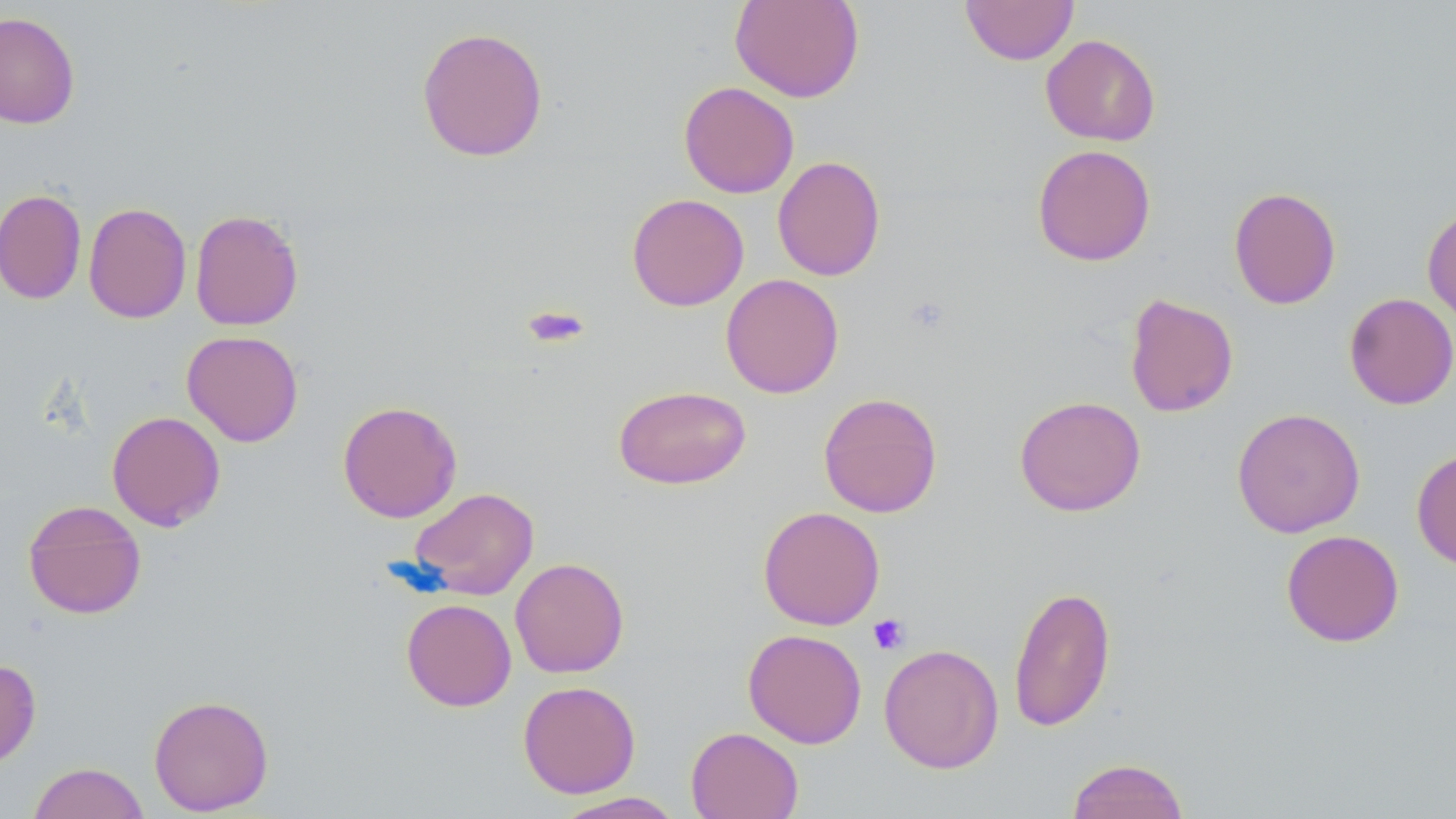
slide_level_diagnosis: no evidence of blood parasites
modality: optical microscopy
preparation: thin blood smear
magnification: 1000x
uninfected_red_blood_cell_locations: 'approximate bounding boxes as (x1,y1)-(x2,y2) corner pairs in pixels: (730,0)-(864,103), (960,0)-(1079,65), (0,11)-(80,129), (416,25)-(549,162), (1040,34)-(1161,146), (678,81)-(799,198), (1032,144)-(1156,267), (772,156)-(886,281), (1228,186)-(1341,309), (0,187)-(86,305), (626,193)-(749,311), (83,202)-(192,324), (1422,205)-(1456,324), (189,209)-(304,331), (720,273)-(844,399), (1344,292)-(1456,409), (1124,293)-(1239,418), (182,330)-(304,447), (613,384)-(751,489), (818,392)-(943,518), (1014,395)-(1146,516), (337,400)-(462,523), (1232,407)-(1365,538), (106,410)-(226,531), (1411,447)-(1456,570), (409,487)-(539,600), (23,500)-(147,619), (758,506)-(885,630), (1281,529)-(1404,647), (509,557)-(630,678), (1008,585)-(1116,732), (401,598)-(517,712), (743,629)-(867,748), (878,644)-(1003,774), (0,659)-(41,769), (518,680)-(640,798), (148,694)-(274,815), (686,726)-(803,819), (1066,757)-(1190,819), (27,762)-(150,819), (554,792)-(685,819)'
platelet_locations: 'approximate bounding boxes as (x1,y1)-(x2,y2) corner pairs in pixels: (521,305)-(592,349), (868,614)-(910,655)'
field_of_view: one of a larger specimen
stain: May-Grünwald-Giemsa
image_size: 1456×819 pixels